Identify the cell.
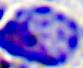
This is a leukocyte.

magnification = 400x
modality = photomicrograph